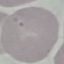 Result: no malaria parasites detected. Automatically extracted cell patch, resized to 64 × 64 pixels. Giemsa stain. Acquired by smartphone through the microscope eyepiece. Thin blood film.